Assess this cell for malaria.
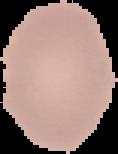
Uninfected.

Image is 118×154 pixels. The area outside the segmented cell region is set to black. From a thin blood film.